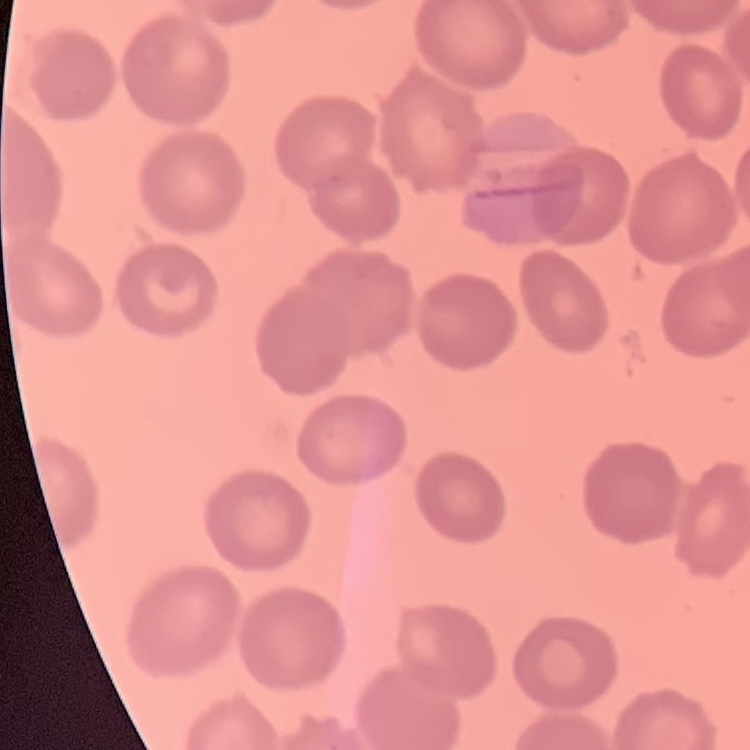 The erythrocytes show no rouleaux formation. Field's or Giemsa stain. One tile cut from a larger photomicrograph. Thin blood smear.